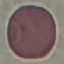

result = negative for malaria parasites
capture = smartphone through the microscope eyepiece
preparation = thin smear
image type = automatically extracted cell patch, resized to 64 × 64 pixels
stain = Giemsa